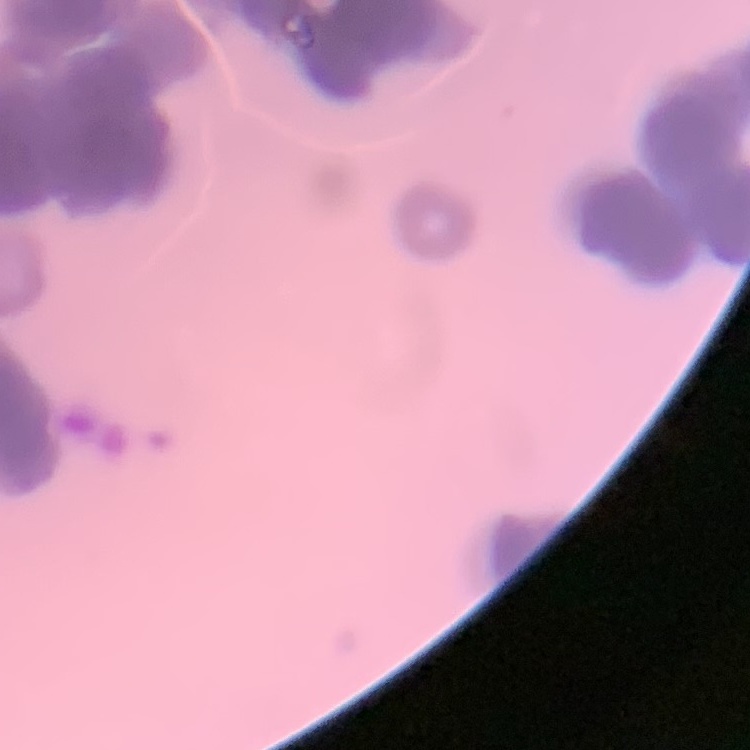
erythrocyte morphology = rouleaux formation
stain = Field's or Giemsa
preparation = thin blood film
image type = one tile cut from a larger photomicrograph